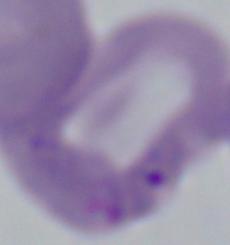

identification: Babesia
magnification: 1000x
modality: photomicrograph